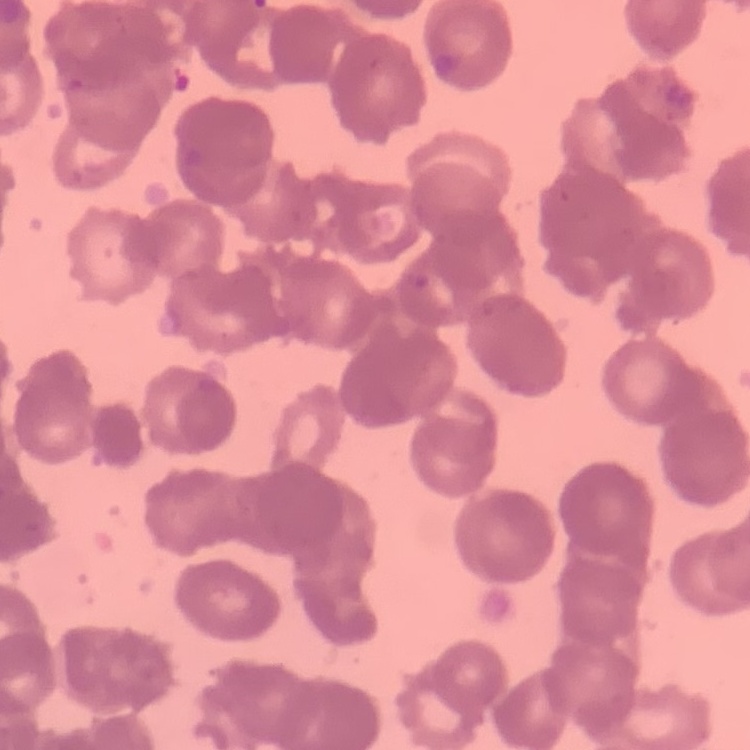
erythrocyte_morphology: rouleaux formation
image_type: one tile cut from a larger photomicrograph
stain: Field's or Giemsa
preparation: thin blood film